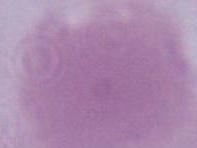

Summary:
  - Identification: erythrocyte
  - Modality: micrograph
  - Magnification: 1000x